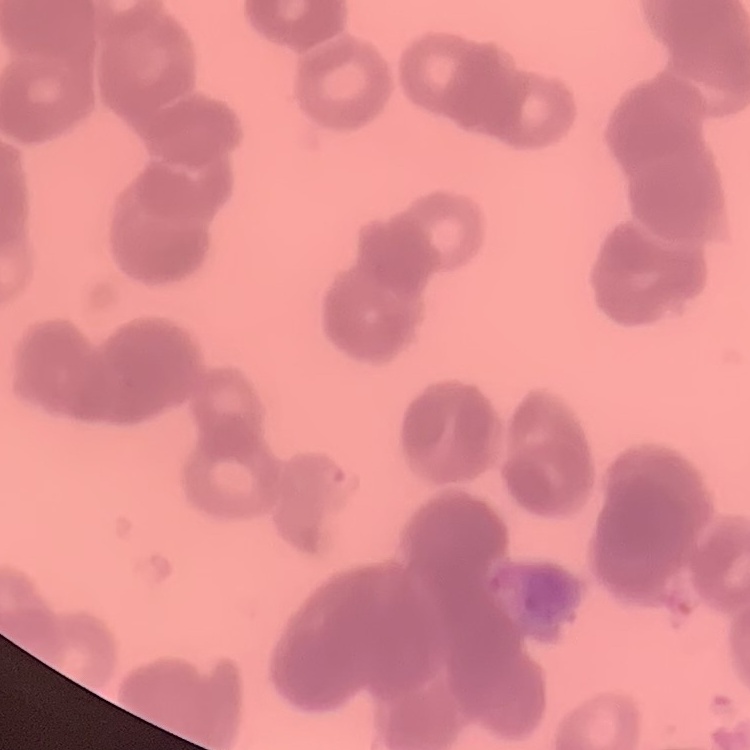

erythrocyte morphology = rouleaux formation
stain = Field's or Giemsa
preparation = thin blood smear
image type = square crop of a larger photomicrograph